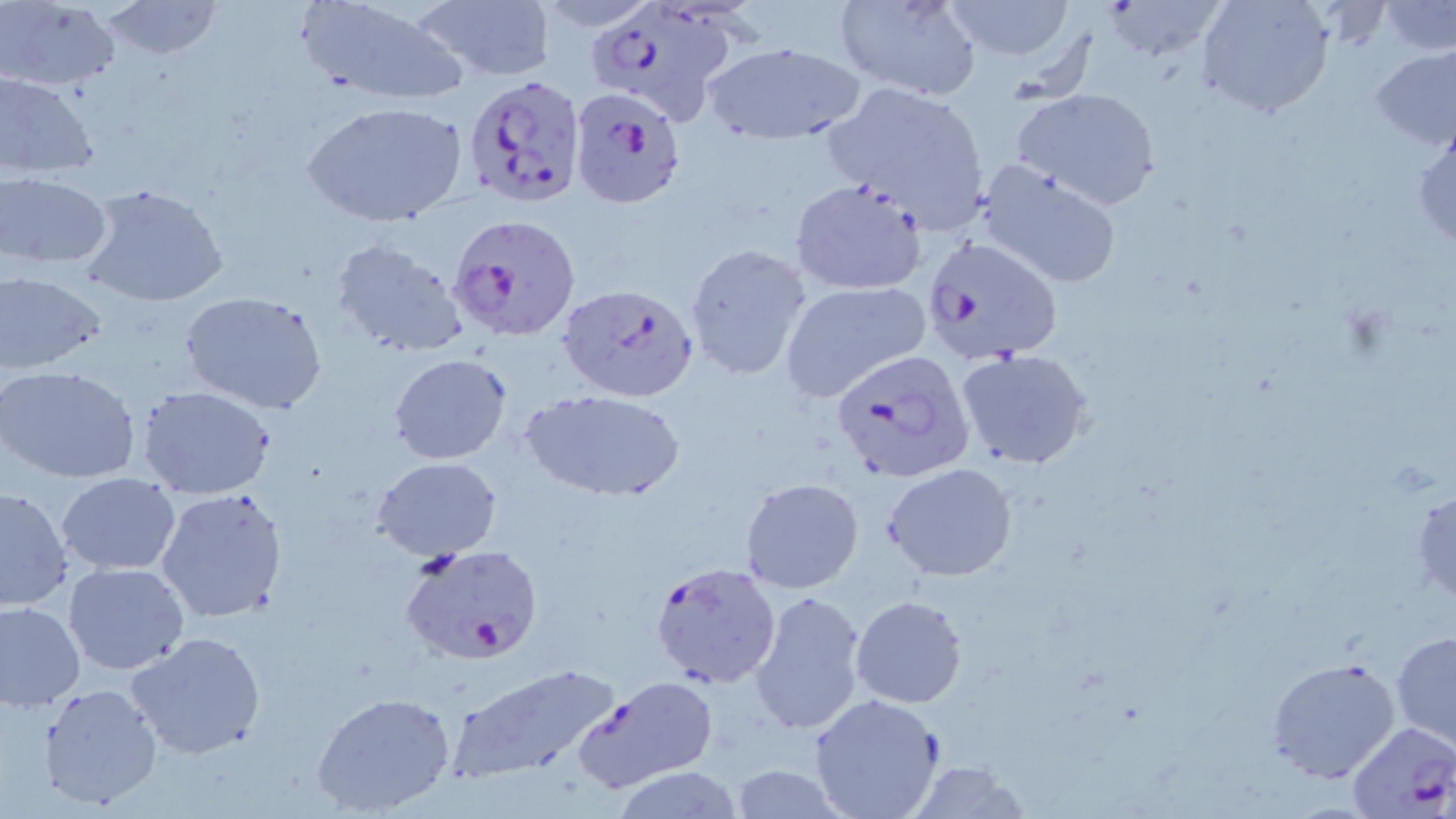

slide_level_diagnosis: Plasmodium falciparum
stain: May-Grünwald-Giemsa
uninfected_red_blood_cell_locations: 'approximate bounding boxes as (x1,y1)-(x2,y2) corner pairs in pixels: (98,0)-(223,63), (298,0)-(469,107), (413,0)-(554,83), (832,0)-(982,100), (939,0)-(1080,61), (1103,0)-(1230,60), (1197,0)-(1333,119), (1,1)-(120,90), (1379,2)-(1456,55), (701,39)-(867,145), (1369,45)-(1456,151), (0,69)-(98,179), (826,83)-(992,229), (1011,86)-(1162,211), (303,98)-(468,229), (1412,119)-(1456,255), (976,158)-(1125,291), (1,172)-(112,270), (788,178)-(927,296), (79,181)-(231,309), (331,236)-(470,359), (684,243)-(814,381), (1,270)-(104,374), (780,281)-(931,403), (178,290)-(329,415), (954,347)-(1095,471), (388,354)-(512,463), (0,365)-(141,483), (136,385)-(277,498), (522,389)-(687,500), (372,457)-(501,561), (883,462)-(1018,581), (57,473)-(181,575), (740,477)-(865,594), (1411,482)-(1456,604), (0,485)-(73,611), (155,486)-(290,626), (64,563)-(189,676), (749,590)-(867,737), (851,596)-(967,708), (0,599)-(85,713), (1391,630)-(1456,750), (125,631)-(267,760), (1264,656)-(1403,784), (446,662)-(624,782), (571,677)-(721,795), (39,684)-(161,810), (311,690)-(457,816), (808,694)-(945,819), (1344,720)-(1456,817), (903,762)-(1029,819), (724,764)-(850,819), (609,767)-(745,818)'
preparation: thin blood smear
plasmodium_falciparum_infected_red_blood_cell_locations: 'approximate bounding boxes as (x1,y1)-(x2,y2) corner pairs in pixels: (586,0)-(739,124), (463,75)-(586,210), (568,86)-(687,210), (449,212)-(579,342), (920,236)-(1065,368), (555,283)-(700,403), (831,350)-(975,483), (402,546)-(543,664), (650,561)-(783,690)'
magnification: 1000x
field_of_view: single
modality: optical microscopy
image_size: 1456×819 pixels